Give the position of every Plasmodium parasite visible.
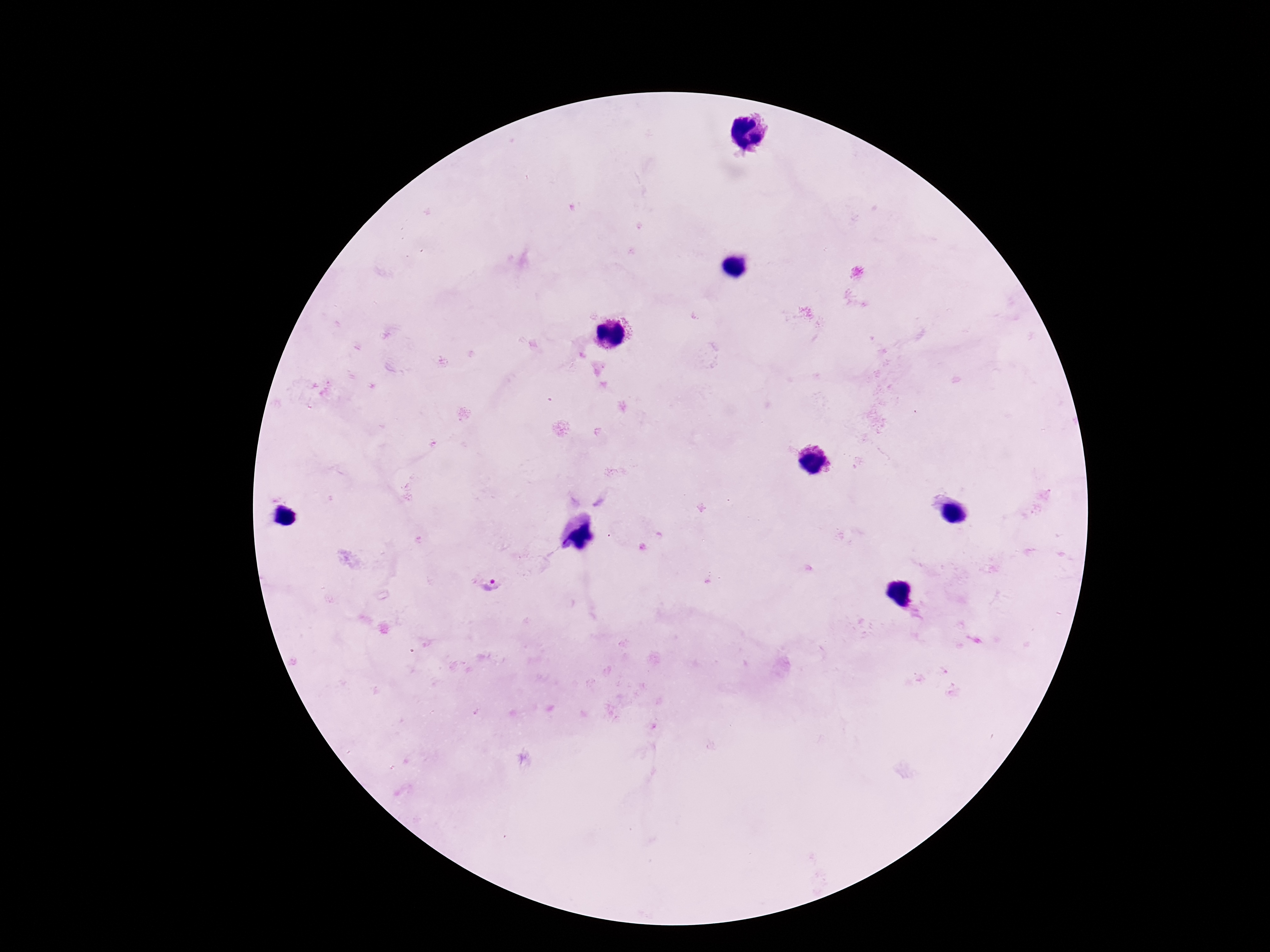
Approximate object centers, in pixels from the top-left corner.
Plasmodium parasites: (x=491, y=585).

{
  "patient_malaria_status": "positive",
  "capture": "smartphone camera through the microscope eyepiece",
  "image_size": "1270×952 pixels",
  "stain": "Giemsa",
  "field_of_view": "one from this slide",
  "preparation": "thick blood smear",
  "magnification": "100x"
}